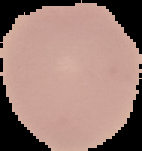

Result: no malaria parasites detected. From a thin blood smear. Segmented cell region on a black background. Image is 142×151 pixels.